Assess the morphology of the red blood cells.
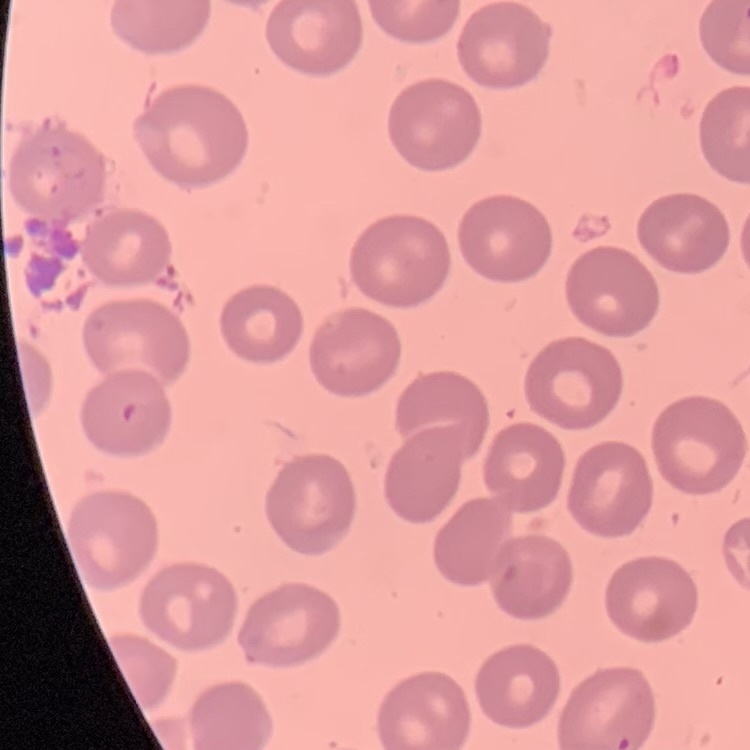
No rouleaux formation.

One tile cut from a larger photomicrograph. Thin blood film. Stained with either Field's or Giemsa.